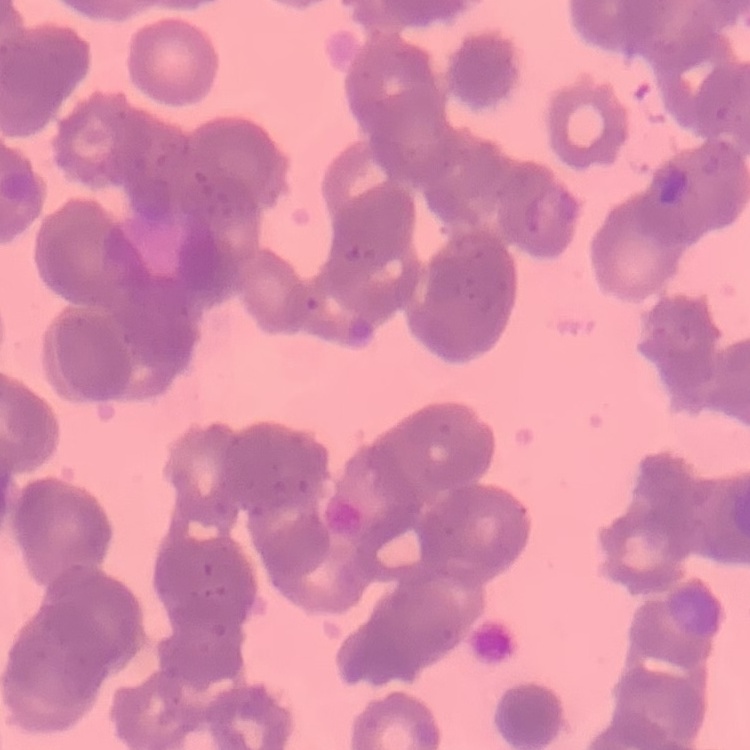

The red blood cells show rouleaux formation. Square crop of a larger photomicrograph. Thin peripheral smear. Field's or Giemsa stain.